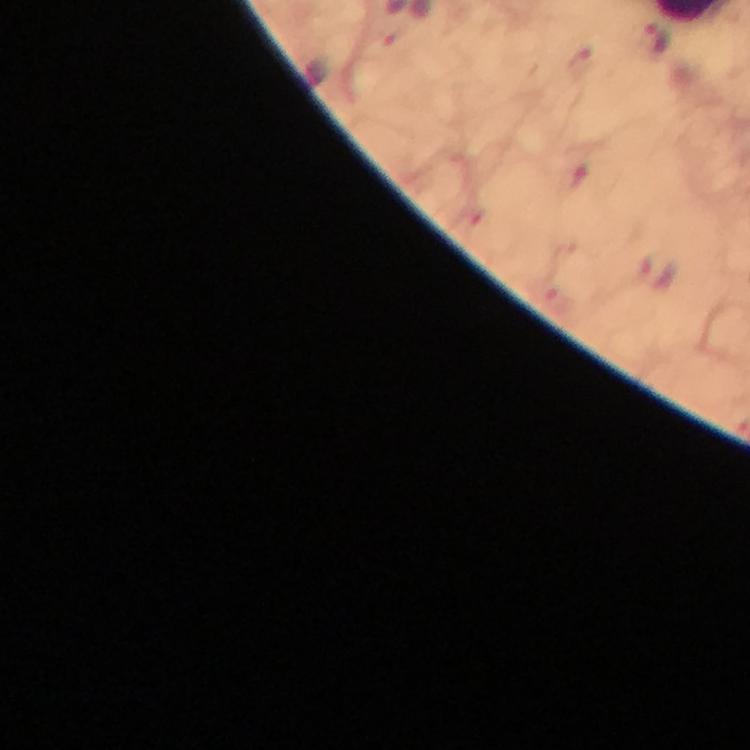

Approximate centers as [x, y] in pixels. Malaria parasite locations: [656, 40], [657, 272]. Thick blood film. Cropped region of a single field of view. Image is 750×750 pixels. 100x magnification. From a malaria diagnostic workup. Smartphone photograph taken through a microscope. Giemsa-stained preparation. Immersion oil applied.